Point out each Plasmodium parasite.
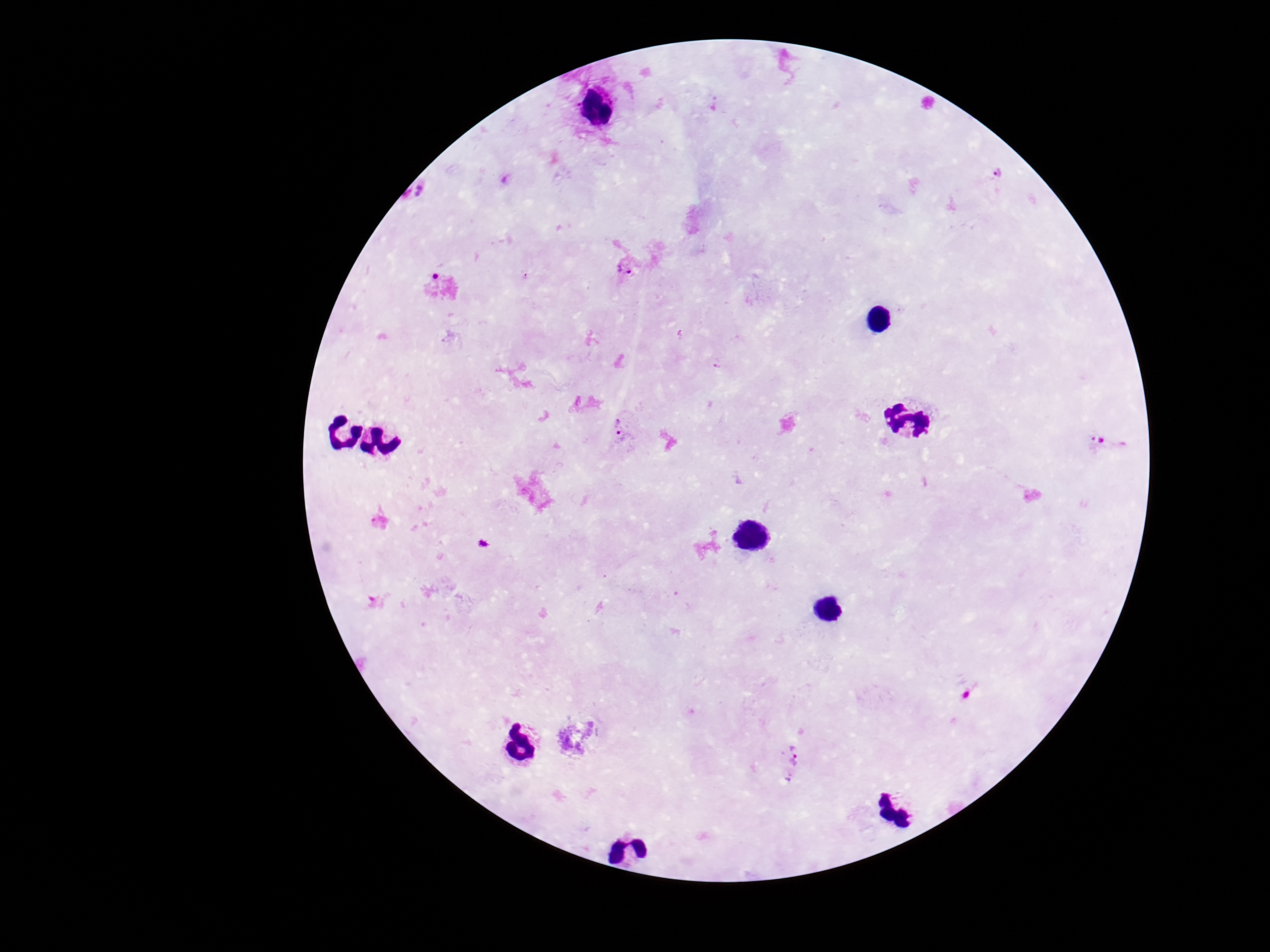
Approximate centers as (x, y) in pixels.
Plasmodium parasites: (1001, 173), (627, 267), (716, 365), (624, 433), (1107, 445), (790, 762).

Single field of view. Giemsa stain. Image is 1270×952 pixels. 100x magnification. Photographed through the microscope eyepiece with a smartphone camera. Patient malaria status: infected. Thick blood film.